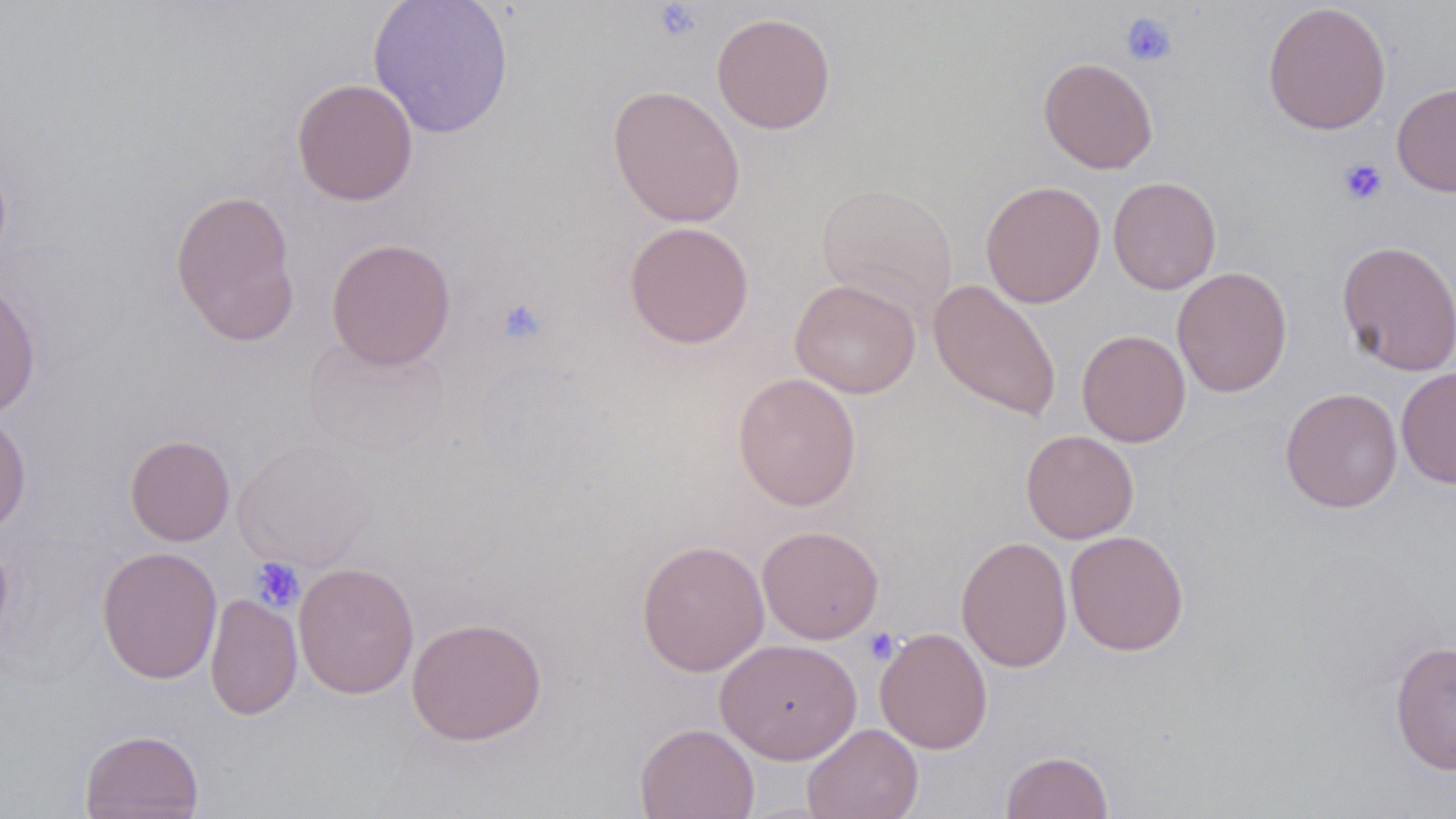
Summary:
  - Coordinate format: approximate bounding boxes as [x1, y1, x2, y2] in pixels
  - Uninfected red blood cell locations: [367, 0, 514, 139], [1262, 1, 1391, 135], [711, 13, 836, 134], [1039, 57, 1158, 174], [291, 78, 419, 206], [1392, 83, 1456, 197], [607, 84, 746, 227], [1107, 176, 1222, 295], [980, 181, 1105, 308], [816, 182, 959, 321], [170, 188, 301, 347], [624, 221, 755, 349], [326, 238, 456, 370], [1336, 239, 1456, 376], [1172, 266, 1293, 397], [789, 278, 921, 398], [928, 278, 1063, 422], [0, 281, 41, 418], [1077, 329, 1191, 447], [302, 334, 451, 460], [466, 351, 627, 492], [1396, 366, 1456, 489], [732, 372, 861, 511], [1280, 387, 1403, 513], [0, 413, 31, 537], [1021, 430, 1139, 544], [124, 434, 235, 545], [232, 438, 376, 571], [757, 525, 884, 644], [1064, 530, 1189, 656], [0, 532, 14, 660], [956, 535, 1072, 673], [636, 539, 770, 677], [96, 545, 223, 684], [293, 562, 419, 699], [204, 593, 302, 720], [406, 616, 547, 746], [875, 627, 993, 754], [714, 638, 863, 764], [1390, 640, 1456, 775], [634, 722, 760, 819], [803, 723, 923, 819], [80, 729, 203, 819], [1000, 750, 1114, 819]
  - Platelet locations: [651, 2, 705, 42], [1120, 13, 1177, 68], [1337, 158, 1388, 206], [495, 297, 549, 345], [250, 557, 304, 612], [863, 627, 900, 664]
  - Slide-level diagnosis: negative for blood parasites
  - Field of view: one of a larger specimen
  - Stain: May-Grünwald-Giemsa
  - Modality: light microscopy
  - Magnification: 1000x
  - Image size: 1456×819 pixels
  - Preparation: thin blood film